Comment on the morphology of the erythrocytes.
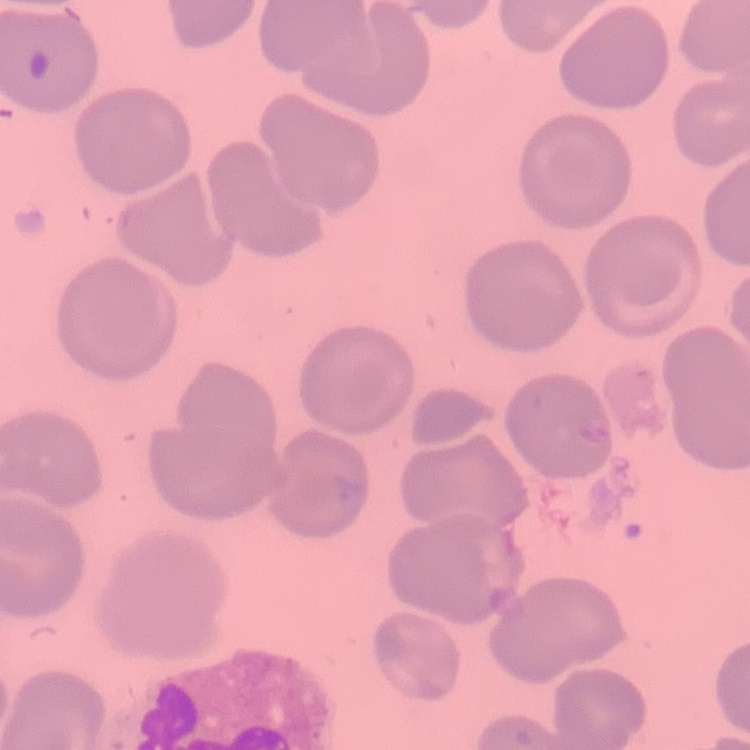

They show no rouleaux formation.

preparation = thin blood film
image type = square crop of a larger photomicrograph
stain = Field's or Giemsa